Describe the morphology of the red blood cells.
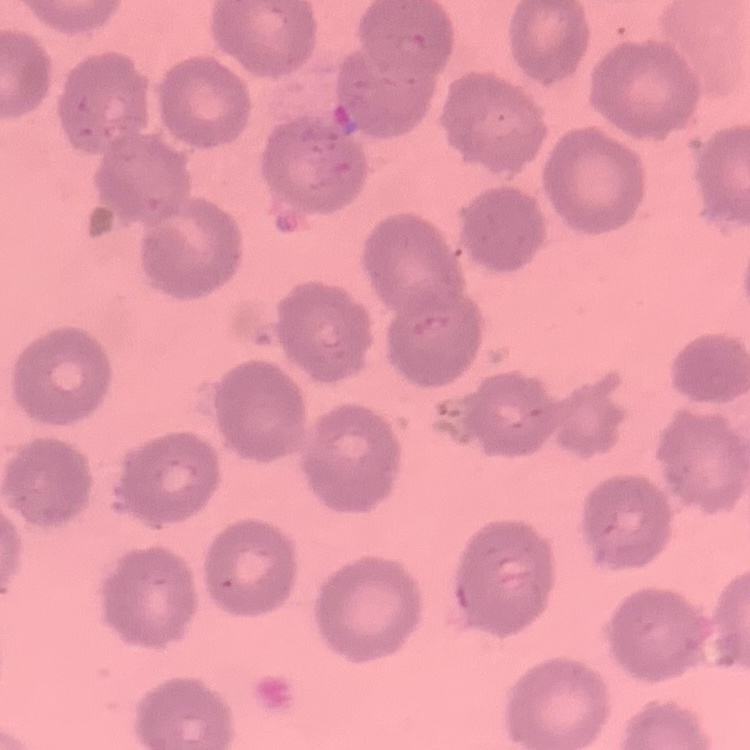

They show no rouleaux formation.

Summary:
  - Preparation: thin blood smear
  - Image type: one tile cut from a larger photomicrograph
  - Stain: Field's or Giemsa